Locate every malaria parasite.
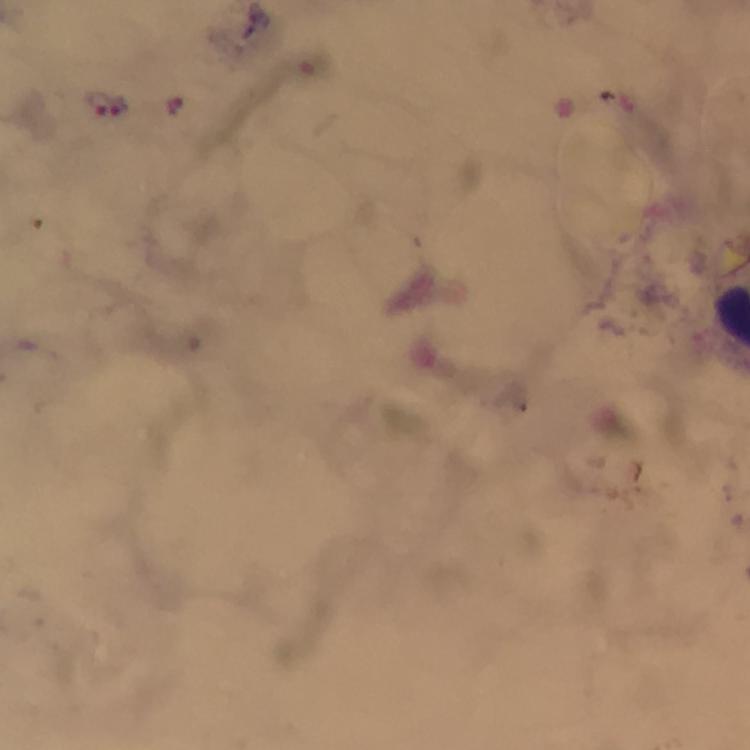
Approximate centers as (x, y) in pixels.
Malaria parasites: (105, 102), (174, 105).

capture = smartphone camera through the microscope
image size = 750×750 pixels
cropped from = one field of view
magnification = 100x
preparation = thick blood smear
immersion oil = used
stain = Giemsa
context = from a diagnostic examination for malaria